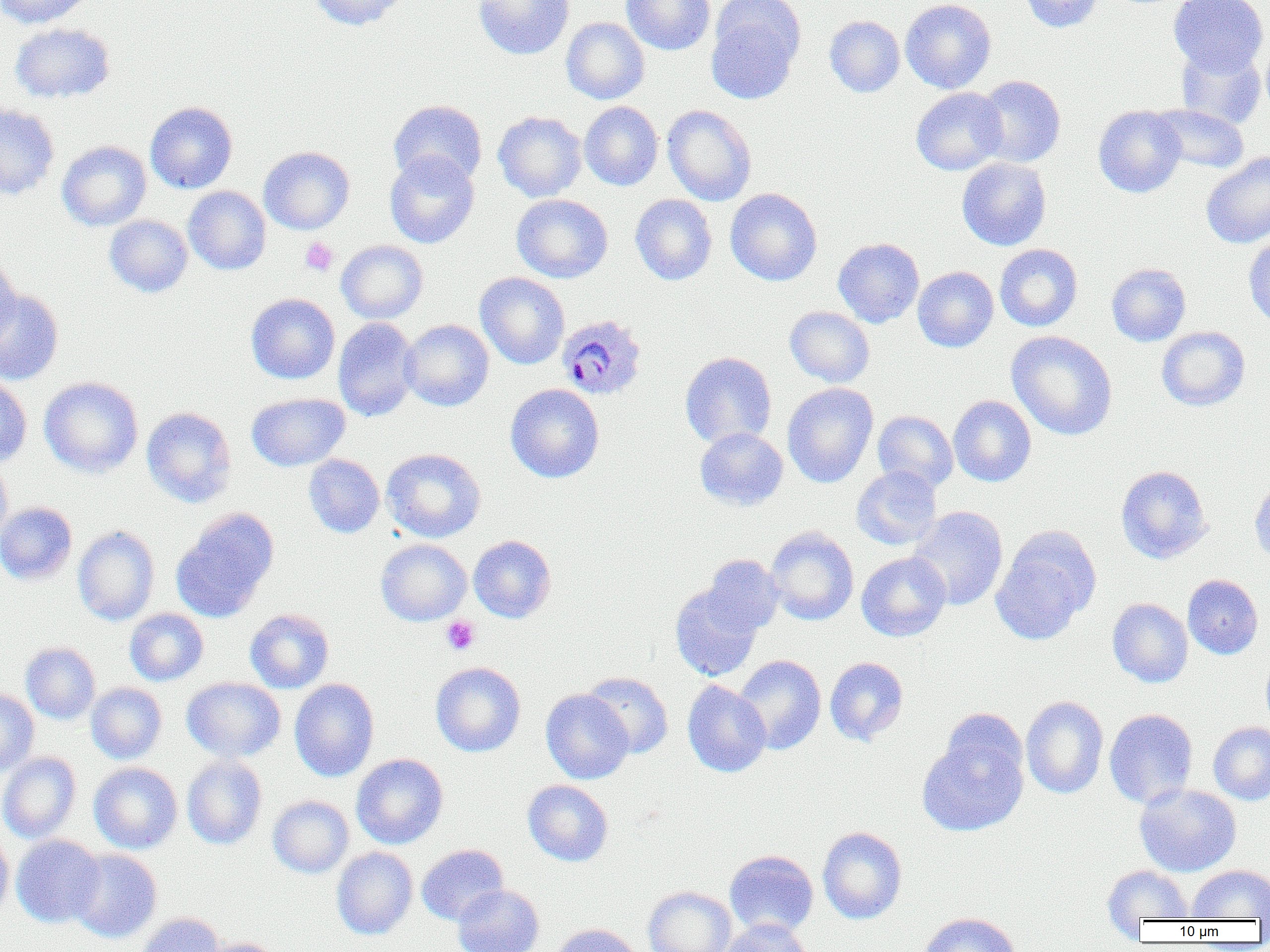

Summary:
  - Coordinate format: approximate bounding boxes as (x1, y1, x2, y2) in pixels
  - Platelet locations: (300, 237, 339, 276), (441, 616, 481, 655)
  - Plasmodium ovale-infected red blood cell locations: (557, 315, 647, 400)
  - Uninfected red blood cell locations: (0, 0, 94, 28), (309, 0, 408, 30), (473, 0, 574, 60), (621, 0, 715, 55), (900, 0, 996, 94), (1018, 0, 1103, 32), (1169, 0, 1269, 76), (706, 3, 803, 104), (825, 15, 905, 98), (561, 17, 649, 104), (570, 17, 655, 190), (10, 23, 114, 103), (1261, 38, 1270, 123), (1176, 44, 1266, 129), (974, 75, 1066, 168), (911, 87, 1008, 176), (388, 99, 487, 187), (145, 101, 238, 193), (579, 102, 663, 191), (0, 103, 59, 200), (1150, 104, 1250, 174), (662, 105, 757, 206), (1093, 105, 1186, 198), (493, 111, 587, 202), (57, 141, 152, 230), (258, 146, 355, 234), (384, 151, 480, 248), (1201, 152, 1270, 248), (957, 157, 1051, 250), (183, 186, 271, 275), (725, 188, 822, 286), (511, 194, 613, 283), (630, 194, 717, 285), (104, 215, 192, 297), (1243, 236, 1270, 329), (833, 238, 924, 327), (336, 240, 428, 324), (995, 244, 1082, 331), (0, 257, 22, 350), (1106, 263, 1191, 346), (913, 266, 999, 353), (475, 272, 570, 369), (0, 289, 64, 385), (246, 293, 340, 384), (785, 306, 875, 387), (333, 317, 420, 421), (400, 319, 494, 411), (1156, 326, 1250, 411), (1007, 331, 1117, 440), (680, 351, 777, 448), (0, 375, 32, 468), (39, 376, 144, 477), (782, 383, 878, 488), (505, 384, 604, 483), (246, 393, 350, 471), (948, 395, 1036, 486), (141, 407, 236, 508), (872, 410, 959, 493), (694, 427, 788, 510), (382, 448, 486, 543), (304, 454, 385, 538), (0, 458, 12, 545), (851, 466, 942, 550), (1116, 466, 1212, 563), (1249, 479, 1270, 565), (0, 502, 77, 585), (908, 506, 1009, 610), (170, 508, 279, 623), (72, 525, 160, 626), (765, 526, 859, 625), (991, 527, 1101, 645), (468, 535, 556, 623), (376, 539, 471, 626), (856, 552, 951, 641), (700, 555, 784, 637), (1183, 574, 1263, 659), (670, 582, 763, 681), (1107, 598, 1193, 688), (125, 608, 209, 686), (245, 609, 334, 693), (21, 642, 100, 723), (1262, 653, 1270, 734), (734, 655, 826, 754), (824, 657, 909, 746), (430, 661, 526, 757), (582, 671, 673, 758), (182, 677, 285, 762), (289, 678, 379, 782), (682, 680, 771, 778), (86, 683, 167, 764), (0, 688, 39, 776), (541, 689, 634, 784), (1021, 696, 1108, 799), (1104, 708, 1199, 808), (919, 718, 1030, 839), (1208, 721, 1270, 805), (0, 751, 80, 843), (352, 754, 449, 849), (182, 756, 267, 850), (89, 763, 182, 854), (523, 780, 613, 866), (1134, 783, 1241, 877), (268, 795, 354, 878), (817, 826, 907, 924), (0, 829, 14, 919), (11, 834, 105, 928), (416, 844, 508, 925), (331, 847, 417, 940), (68, 848, 161, 942), (724, 850, 819, 937), (1186, 864, 1270, 920), (1103, 865, 1193, 922), (453, 883, 544, 952), (643, 886, 737, 952), (917, 912, 1022, 952), (135, 913, 226, 952), (720, 919, 815, 952), (551, 923, 644, 952), (203, 937, 284, 952)
  - Slide-level diagnosis: Plasmodium ovale
  - Magnification: 1000x
  - Field of view: one of a larger specimen
  - Preparation: thin blood film
  - Modality: optical microscopy
  - Image size: 1270×952 pixels